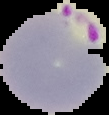
Malaria status: parasitized. The area outside the segmented cell region is set to black. From a thin blood smear. Image is 109×115 pixels.